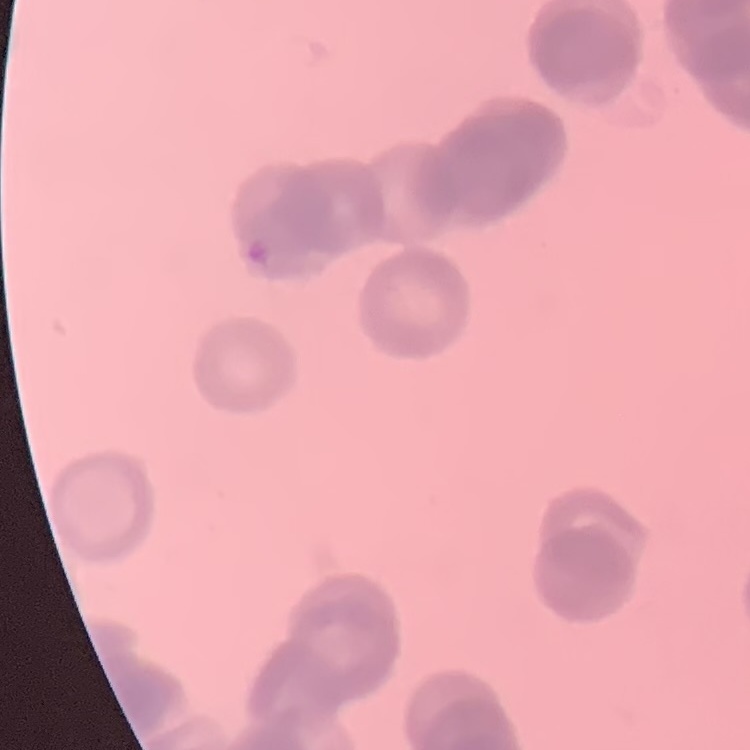

The red blood cells exhibit rouleaux formation. Thin blood film. One tile cut from a larger photomicrograph. Field's or Giemsa stain.